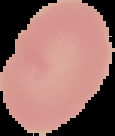 Result: negative for Plasmodium parasites. Image is 115×136 pixels. Segmented cell region on a black background. From a thin blood smear.